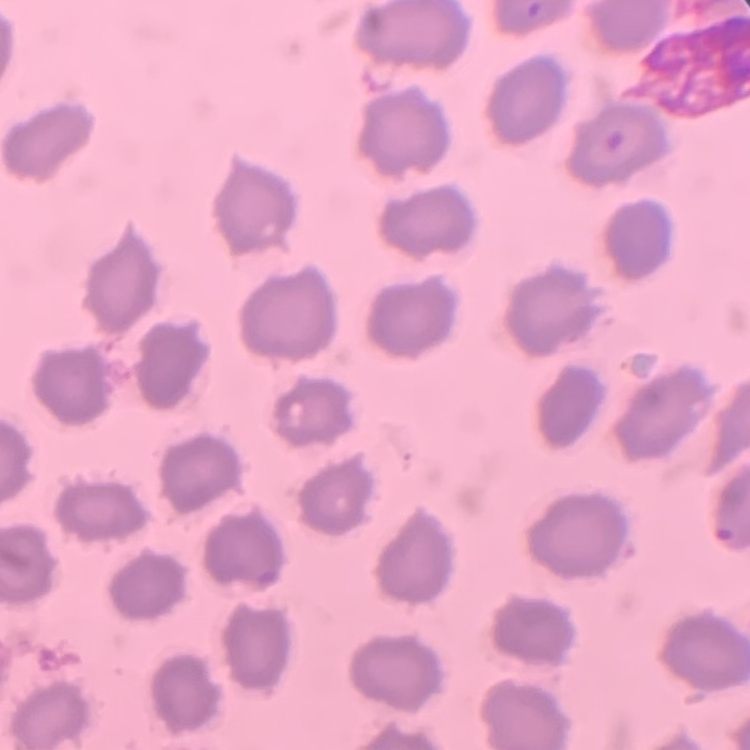
erythrocyte morphology = no rouleaux formation
image type = square crop of a larger photomicrograph
stain = Field's or Giemsa
preparation = thin blood smear